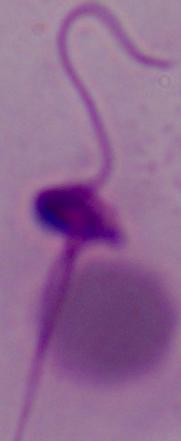

A Leishmania parasite is seen. 1000x magnification. Photomicrograph.